Assess this cell for malaria.
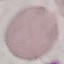

It is uninfected.

Summary:
  - Image type: automatically extracted cell patch, resized to 64 × 64 pixels
  - Capture: smartphone through the microscope eyepiece
  - Preparation: thin blood film
  - Stain: Giemsa